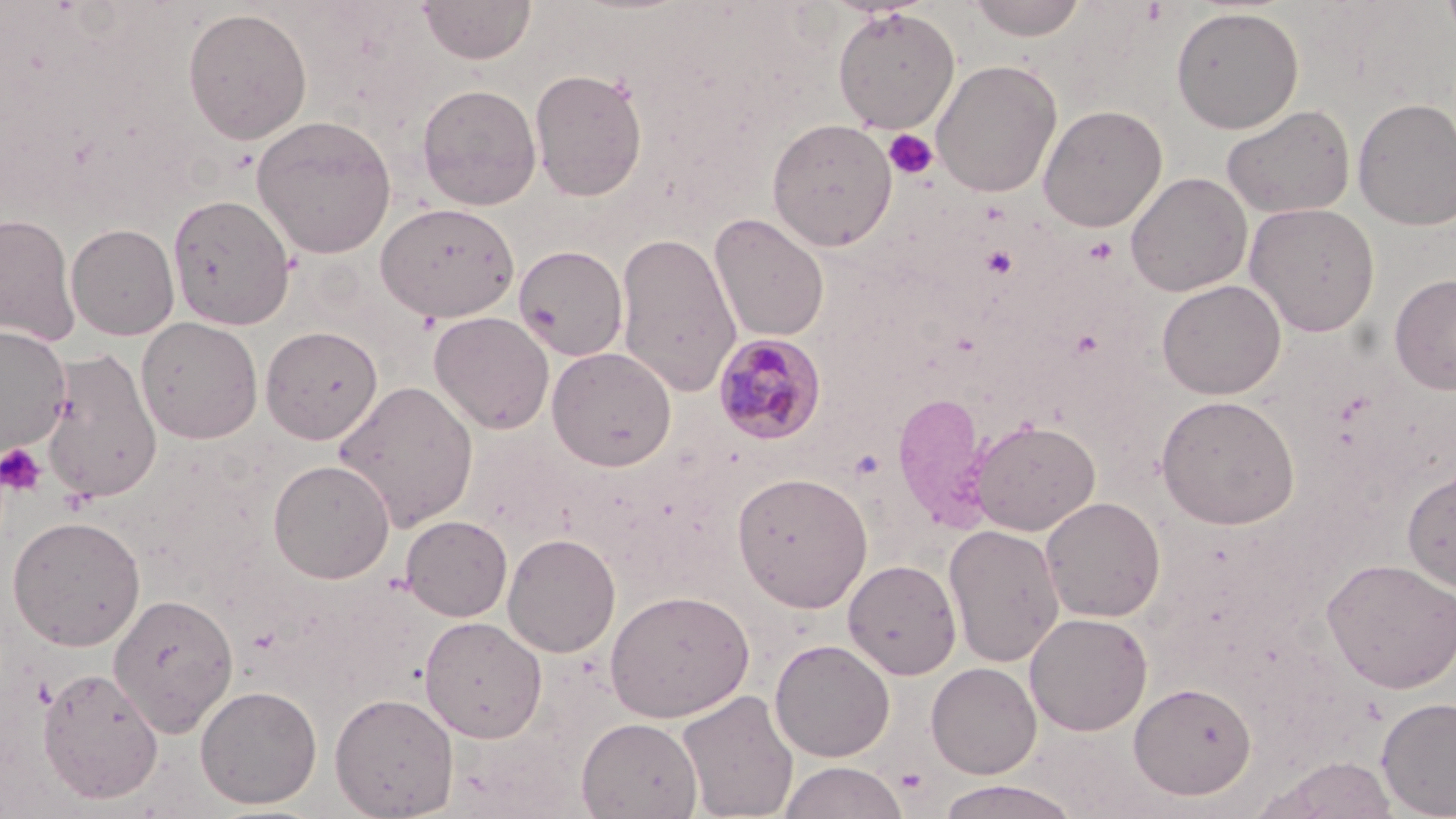
slide-level diagnosis = Plasmodium malariae
field of view = one of a larger specimen
platelet locations = approximate bounding boxes as (x1,y1)-(x2,y2) corner pairs in pixels: (883,128)-(939,181), (980,245)-(1018,278), (1,444)-(45,497), (894,768)-(930,796)
image size = 1456×819 pixels
stain = May-Grünwald-Giemsa
modality = light microscopy
preparation = thin blood smear
Plasmodium malariae-infected red blood cell locations = approximate bounding boxes as (x1,y1)-(x2,y2) corner pairs in pixels: (714,333)-(827,446)
uninfected red blood cell locations = approximate bounding boxes as (x1,y1)-(x2,y2) corner pairs in pixels: (417,0)-(536,64), (966,0)-(1087,41), (1439,0)-(1456,47), (832,6)-(961,133), (1170,6)-(1304,133), (183,7)-(312,145), (931,59)-(1062,198), (529,67)-(648,201), (416,83)-(542,211), (1352,97)-(1456,231), (1038,104)-(1167,232), (1221,104)-(1355,219), (251,114)-(397,258), (766,118)-(897,251), (1125,172)-(1252,297), (167,193)-(296,330), (375,202)-(520,322), (1244,202)-(1380,337), (0,212)-(79,346), (709,213)-(830,342), (66,223)-(180,340), (614,231)-(742,396), (514,244)-(629,361), (1389,274)-(1456,396), (1156,279)-(1286,399), (429,311)-(555,434), (136,316)-(263,444), (0,325)-(71,453), (260,325)-(383,444), (547,347)-(676,471), (40,348)-(163,504), (332,379)-(479,532), (891,390)-(991,529), (1156,394)-(1299,529), (969,419)-(1100,536), (267,459)-(396,584), (1402,467)-(1456,593), (731,471)-(873,612), (1040,496)-(1166,622), (6,515)-(146,650), (400,515)-(512,622), (944,523)-(1065,667), (502,532)-(620,658), (1321,557)-(1456,693), (844,559)-(962,680), (604,589)-(754,723), (108,592)-(239,736), (1025,612)-(1153,735), (419,616)-(548,742), (769,638)-(895,762), (926,662)-(1041,779), (38,665)-(163,805), (1129,681)-(1257,799), (195,684)-(322,809), (677,688)-(799,819), (329,692)-(459,818), (1376,696)-(1456,818), (577,716)-(703,818), (1258,755)-(1401,819), (777,761)-(909,819), (934,780)-(1084,819)
magnification = 1000x